State the preparation type.
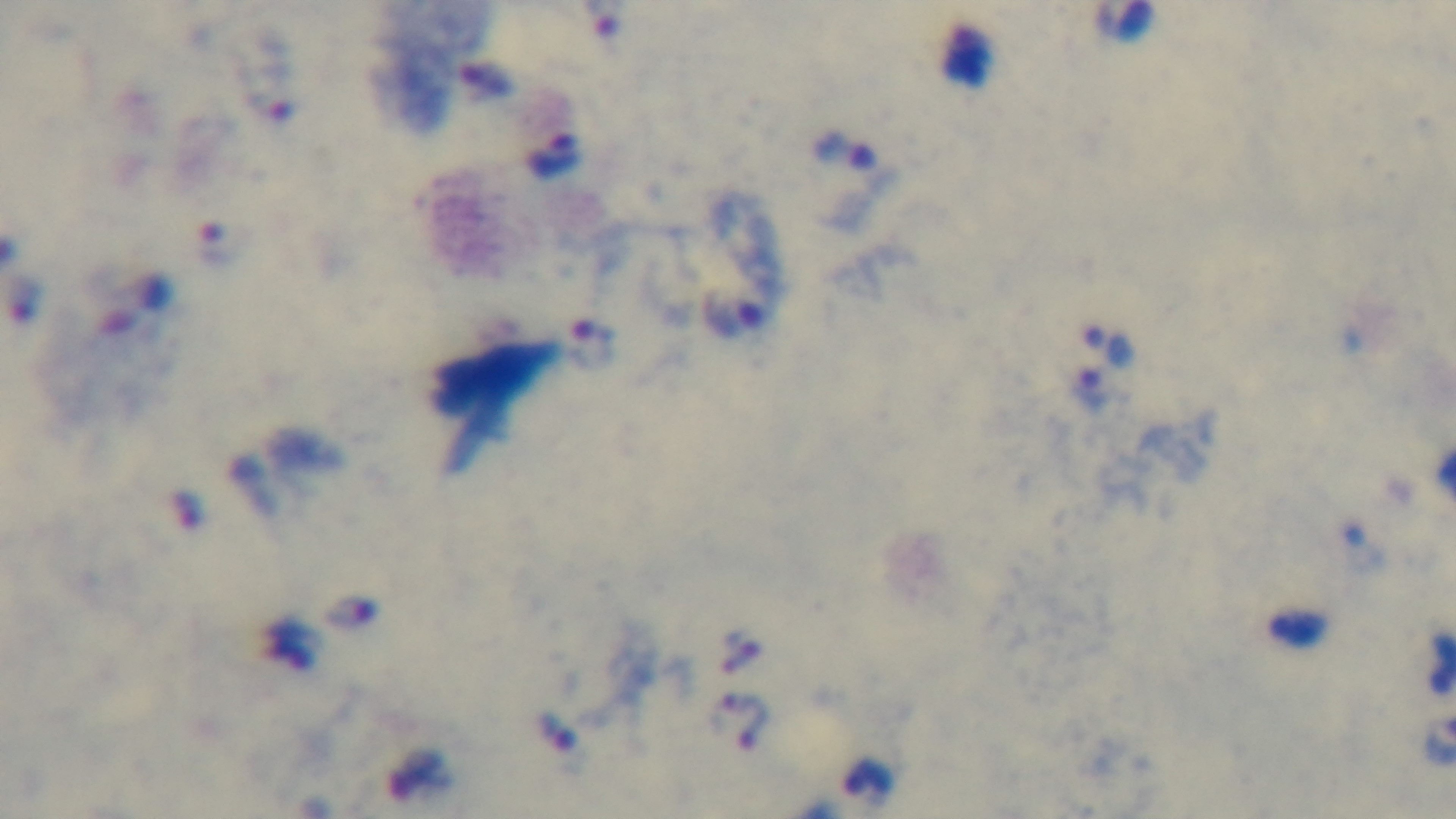

Thick.

Mounted 4K digital camera. One field from the slide. Giemsa stain. 100x oil-immersion objective. Photomicrograph. Malaria status: infected.